Report the malaria status.
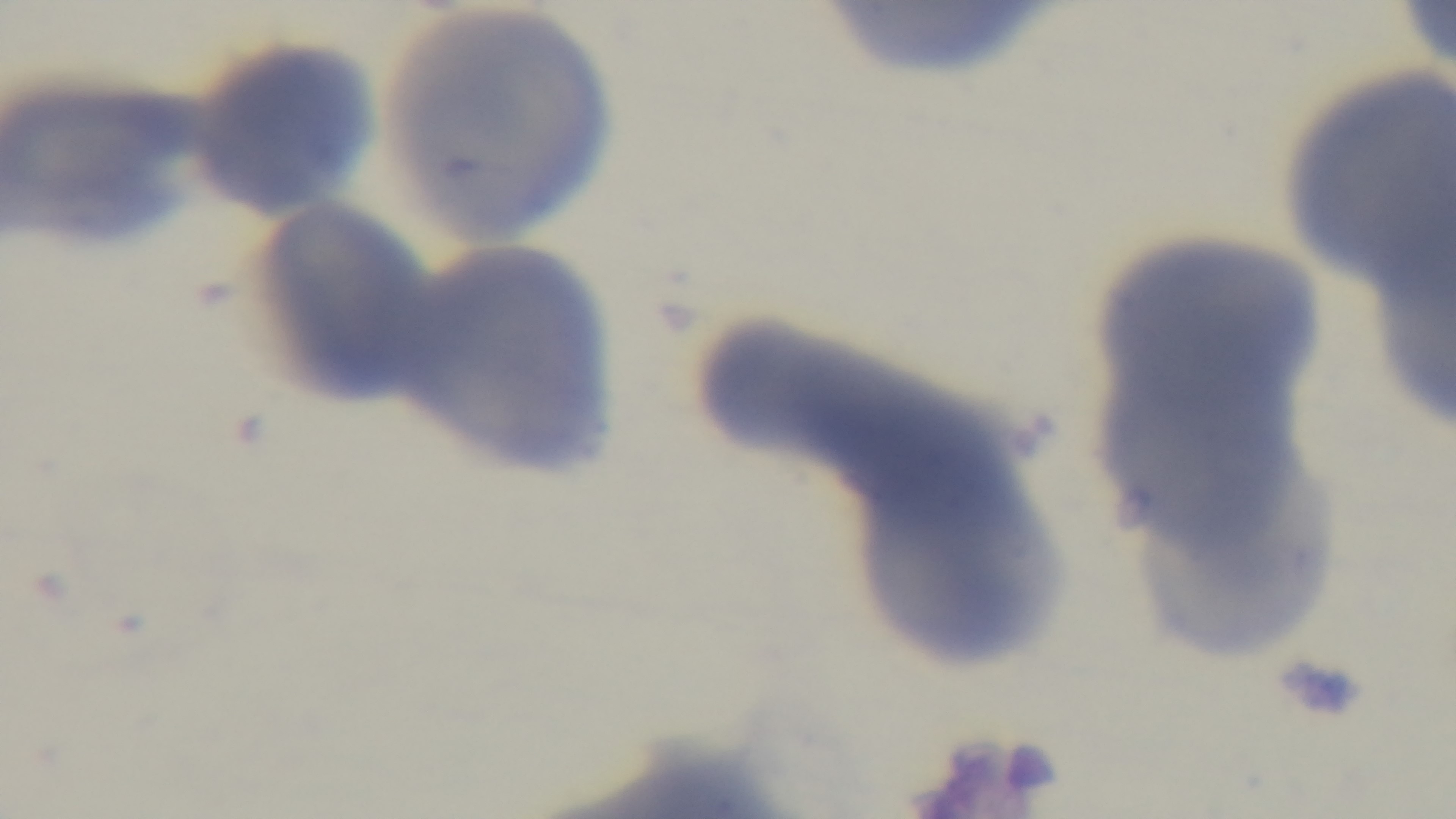

Negative.

Oil-immersion objective, 100x. Preparation: thin blood film. One field from the slide. Mounted 4K digital camera. Giemsa-stained. Light microscopy.